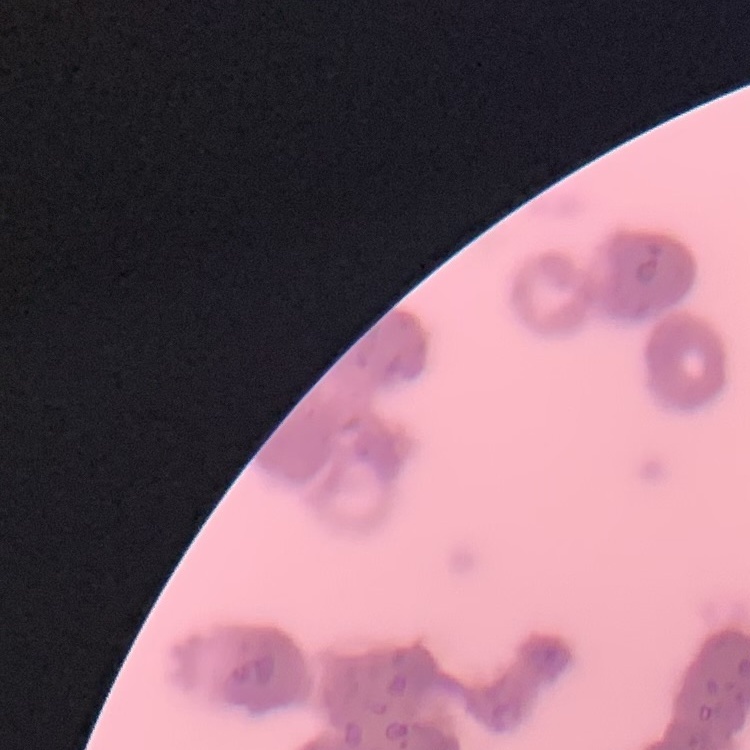

erythrocyte_morphology: rouleaux formation
image_type: square crop of a larger photomicrograph
stain: Field's or Giemsa
preparation: thin blood film